Classify this cell by malaria status.
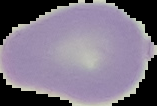

Uninfected.

Summary:
  - Preparation: thin blood smear
  - Image type: segmented cell region with the area outside set to black
  - Image size: 157×106 pixels